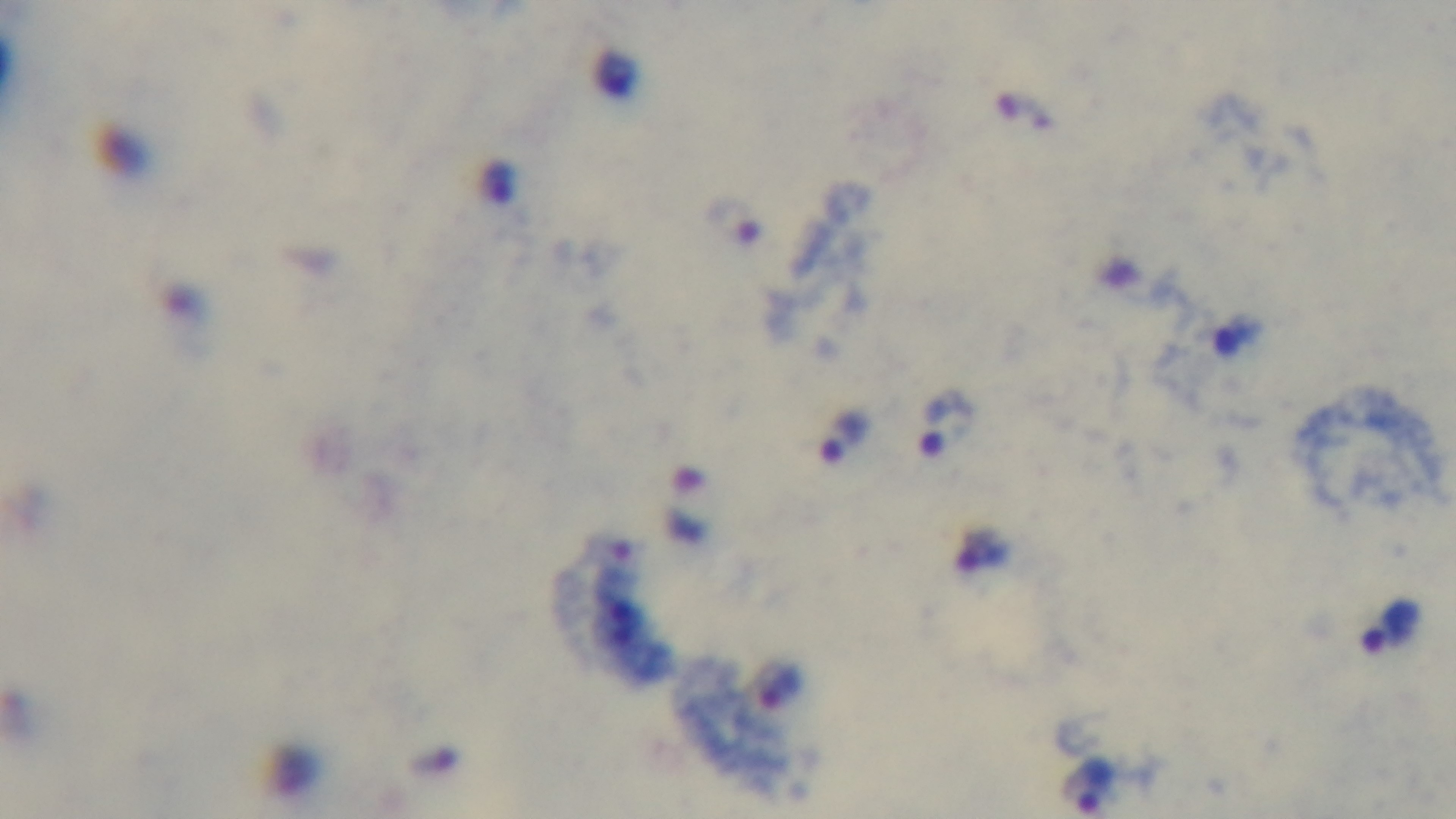

Summary:
  - Stain: Giemsa
  - Preparation: thick smear
  - Modality: light microscopy
  - Malaria status: positive
  - Field of view: single
  - Objective: 100x oil immersion
  - Capture: mounted 4K digital camera